Assess the morphology of the red blood cells.
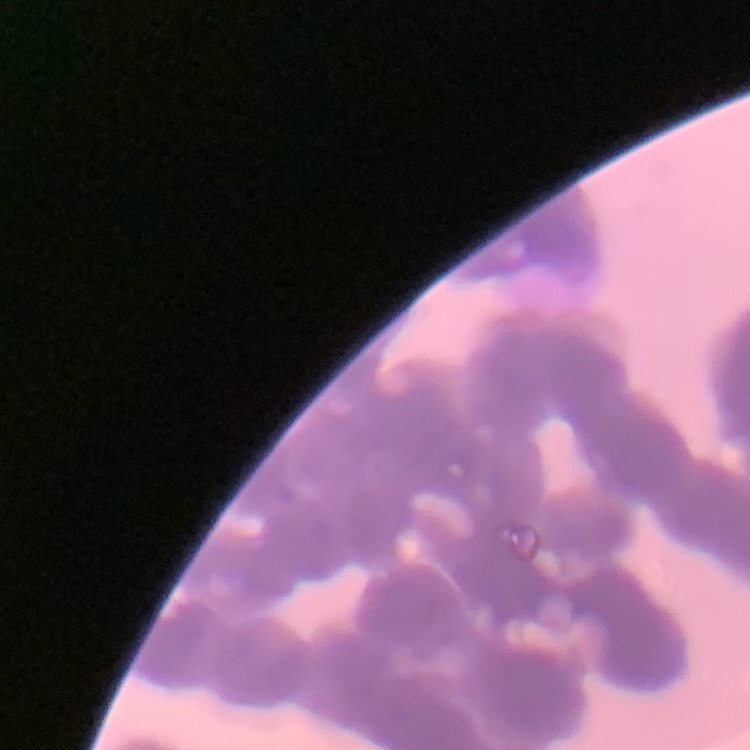
They show rouleaux formation.

Thin blood smear. Square crop of a larger photomicrograph. Stained with either Field's or Giemsa.